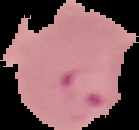

Summary:
  - Image size: 139×130 pixels
  - Image type: cell region segmented out of the field of view; surrounding area masked to black
  - Preparation: thin blood film
  - Malaria status: parasitized